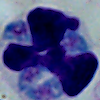
Captured at 1000x magnification. A leukocyte is seen. Photomicrograph.